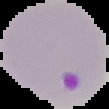

image type = segmented cell region on a black background
image size = 109×109 pixels
malaria status = parasitized
preparation = thin blood smear